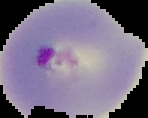
Cell region segmented out of the field of view; the surrounding area is masked to black. From a thin blood film. Image is 148×118 pixels. Malaria status: parasitized.